Name the blood parasite species.
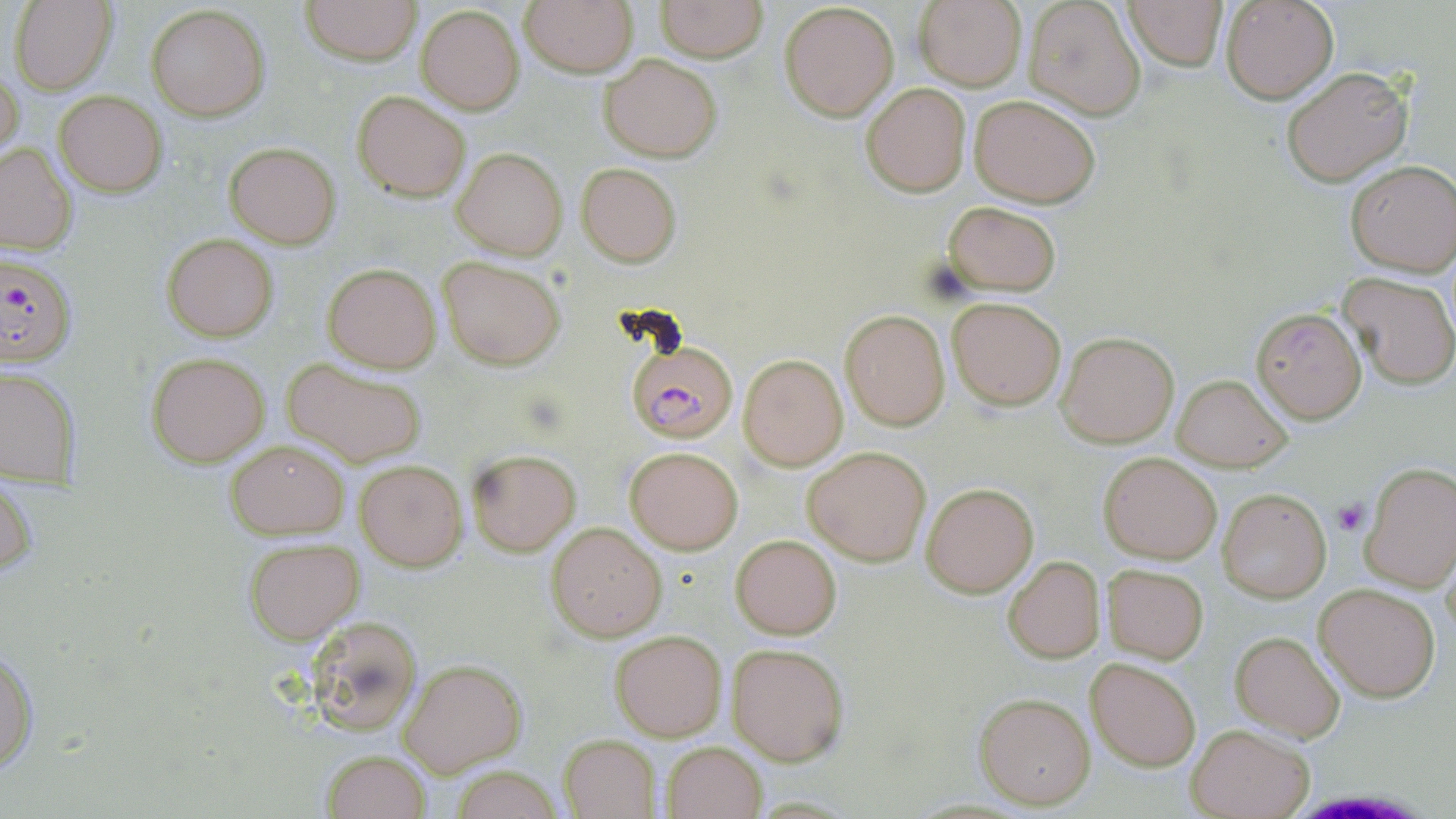

Plasmodium falciparum.

Summary:
  - Coordinate format: approximate bounding boxes as named x1/y1/x2/y2 corners in pixels
  - Platelet locations: (x1=1332, y1=497, x2=1368, y2=536)
  - Uninfected red blood cell locations: (x1=10, y1=0, x2=118, y2=95), (x1=301, y1=0, x2=420, y2=65), (x1=518, y1=0, x2=639, y2=75), (x1=657, y1=0, x2=767, y2=61), (x1=1221, y1=0, x2=1339, y2=103), (x1=913, y1=1, x2=1026, y2=89), (x1=1021, y1=1, x2=1147, y2=120), (x1=1122, y1=1, x2=1229, y2=73), (x1=779, y1=2, x2=900, y2=120), (x1=145, y1=4, x2=269, y2=121), (x1=416, y1=4, x2=525, y2=114), (x1=599, y1=54, x2=720, y2=161), (x1=1, y1=65, x2=23, y2=163), (x1=1279, y1=65, x2=1414, y2=188), (x1=862, y1=82, x2=970, y2=197), (x1=352, y1=89, x2=470, y2=201), (x1=55, y1=92, x2=166, y2=197), (x1=969, y1=94, x2=1101, y2=206), (x1=224, y1=141, x2=340, y2=248), (x1=0, y1=142, x2=77, y2=255), (x1=452, y1=147, x2=567, y2=260), (x1=1344, y1=161, x2=1455, y2=275), (x1=576, y1=162, x2=681, y2=266), (x1=943, y1=201, x2=1062, y2=295), (x1=162, y1=234, x2=278, y2=342), (x1=439, y1=255, x2=566, y2=370), (x1=323, y1=263, x2=440, y2=372), (x1=1339, y1=272, x2=1456, y2=388), (x1=947, y1=298, x2=1065, y2=410), (x1=1250, y1=306, x2=1366, y2=424), (x1=840, y1=310, x2=951, y2=430), (x1=1056, y1=331, x2=1178, y2=447), (x1=146, y1=351, x2=272, y2=467), (x1=738, y1=354, x2=848, y2=471), (x1=281, y1=358, x2=427, y2=467), (x1=1, y1=364, x2=79, y2=489), (x1=1171, y1=373, x2=1290, y2=472), (x1=225, y1=437, x2=350, y2=540), (x1=626, y1=445, x2=744, y2=554), (x1=802, y1=446, x2=931, y2=567), (x1=466, y1=448, x2=580, y2=555), (x1=1098, y1=451, x2=1222, y2=563), (x1=355, y1=458, x2=466, y2=570), (x1=1360, y1=461, x2=1456, y2=593), (x1=1, y1=473, x2=37, y2=582), (x1=922, y1=483, x2=1038, y2=597), (x1=1218, y1=489, x2=1331, y2=603), (x1=547, y1=522, x2=666, y2=641), (x1=731, y1=535, x2=841, y2=639), (x1=243, y1=538, x2=364, y2=642), (x1=1003, y1=556, x2=1103, y2=663), (x1=1102, y1=564, x2=1208, y2=663), (x1=1313, y1=582, x2=1441, y2=702), (x1=307, y1=615, x2=425, y2=739), (x1=610, y1=629, x2=726, y2=741), (x1=1231, y1=632, x2=1346, y2=744), (x1=728, y1=643, x2=849, y2=764), (x1=1, y1=645, x2=37, y2=775), (x1=1085, y1=655, x2=1202, y2=771), (x1=398, y1=659, x2=526, y2=775), (x1=972, y1=690, x2=1095, y2=809), (x1=1185, y1=724, x2=1314, y2=819), (x1=559, y1=734, x2=659, y2=817), (x1=661, y1=740, x2=767, y2=818), (x1=321, y1=748, x2=430, y2=819), (x1=449, y1=766, x2=566, y2=819)
  - Plasmodium falciparum-infected red blood cell locations: (x1=0, y1=251, x2=78, y2=369), (x1=623, y1=327, x2=741, y2=449)
  - Magnification: 1000x
  - Stain: May-Grünwald-Giemsa
  - Field of view: one of a larger specimen
  - Image size: 1456×819 pixels
  - Preparation: thin blood smear
  - Modality: light microscopy